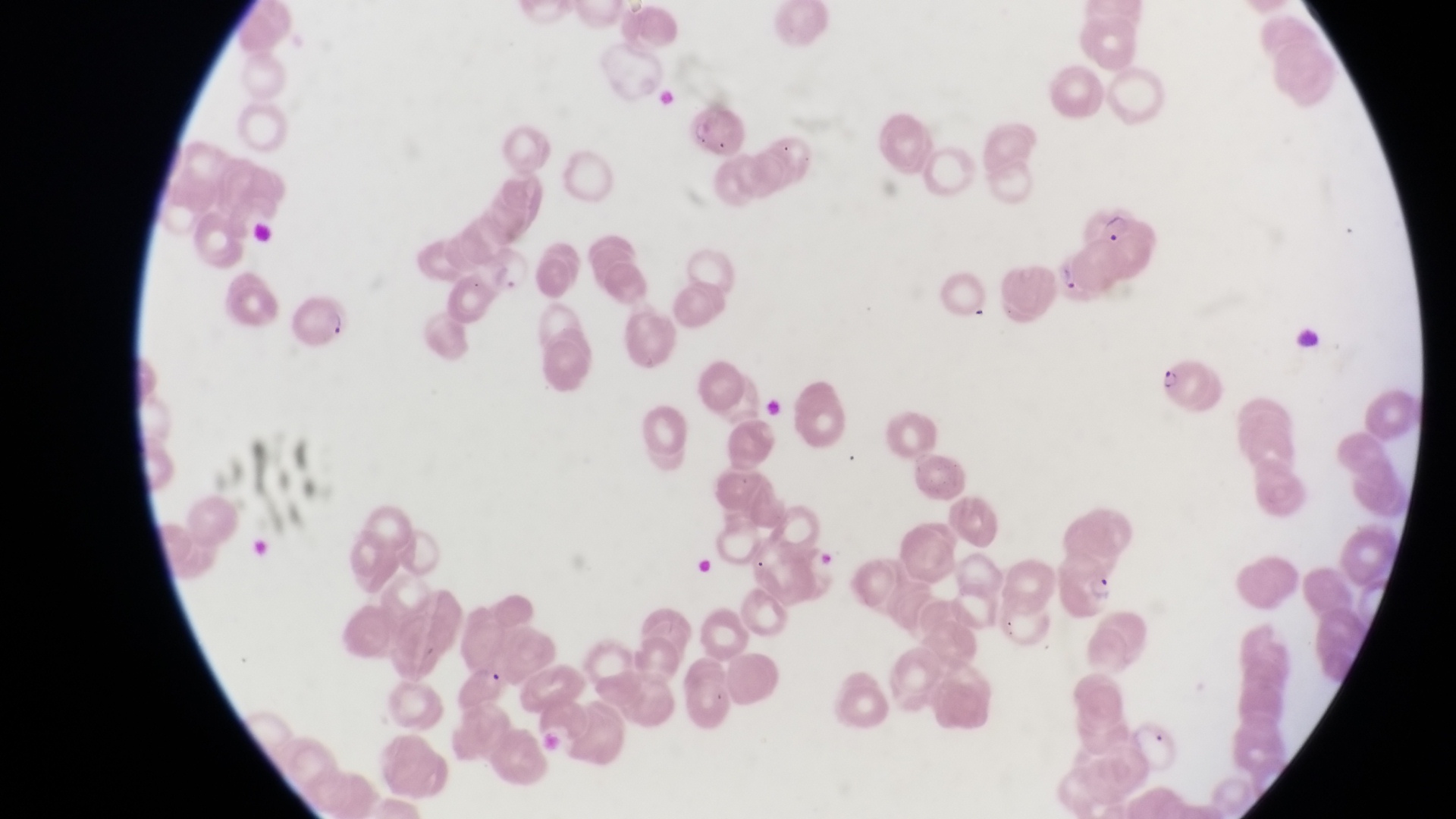

Approximate bounding boxes as {left, top, right, bottom} in pixels.
Summary:
  - Parasitised red blood cell locations: {682, 102, 745, 161}, {293, 290, 351, 350}, {1159, 357, 1209, 406}, {1060, 557, 1126, 620}, {457, 664, 516, 713}
  - Artifact (platelet-like body, stain precipitate, or debris) locations: {479, 238, 534, 291}
  - Trophozoite locations: {1086, 204, 1131, 246}
  - Field of view: single
  - Preparation: thin blood smear
  - Capture: smartphone photograph through the eyepiece of an Olympus CX-23 microscope
  - Country: Uganda
  - Image size: 1456×819 pixels
  - Magnification: 1000x